Comment on the morphology of the erythrocytes.
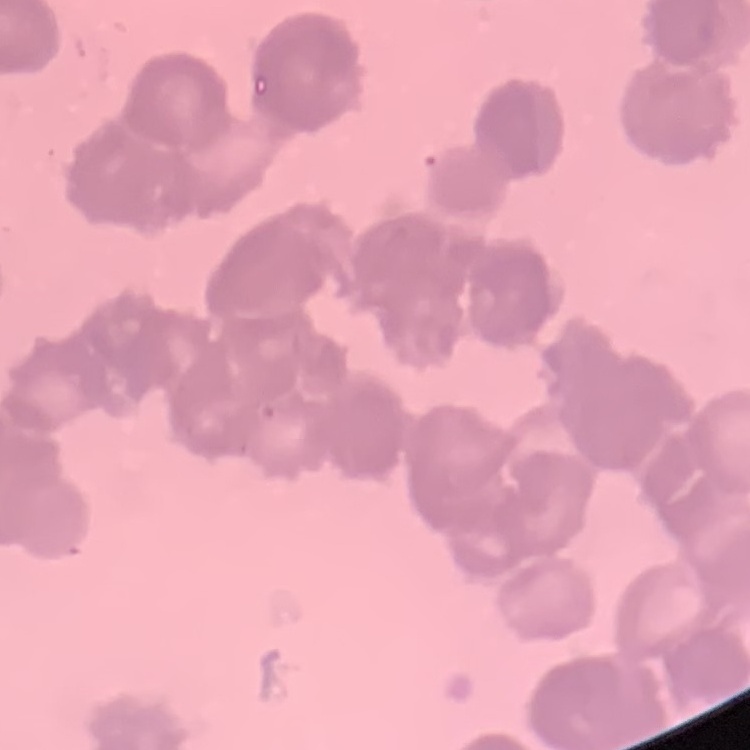

They show rouleaux formation.

image type = square crop of a larger photomicrograph
preparation = thin peripheral smear
stain = Field's or Giemsa